State which parasite is depicted.
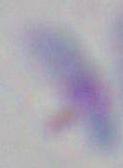
This is Toxoplasma gondii.

Captured at 1000x magnification. Micrograph.